Report the malaria status of this cell.
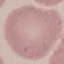

It is uninfected.

capture: smartphone through the microscope eyepiece
stain: Giemsa
preparation: thin blood smear
image_type: automatically extracted cell patch, resized to 64 × 64 pixels